Assess this cell for malaria.
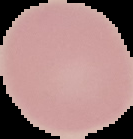
It is uninfected.

{
  "image_size": "133×139 pixels",
  "image_type": "segmented cell region with the area outside set to black",
  "preparation": "thin blood smear"
}